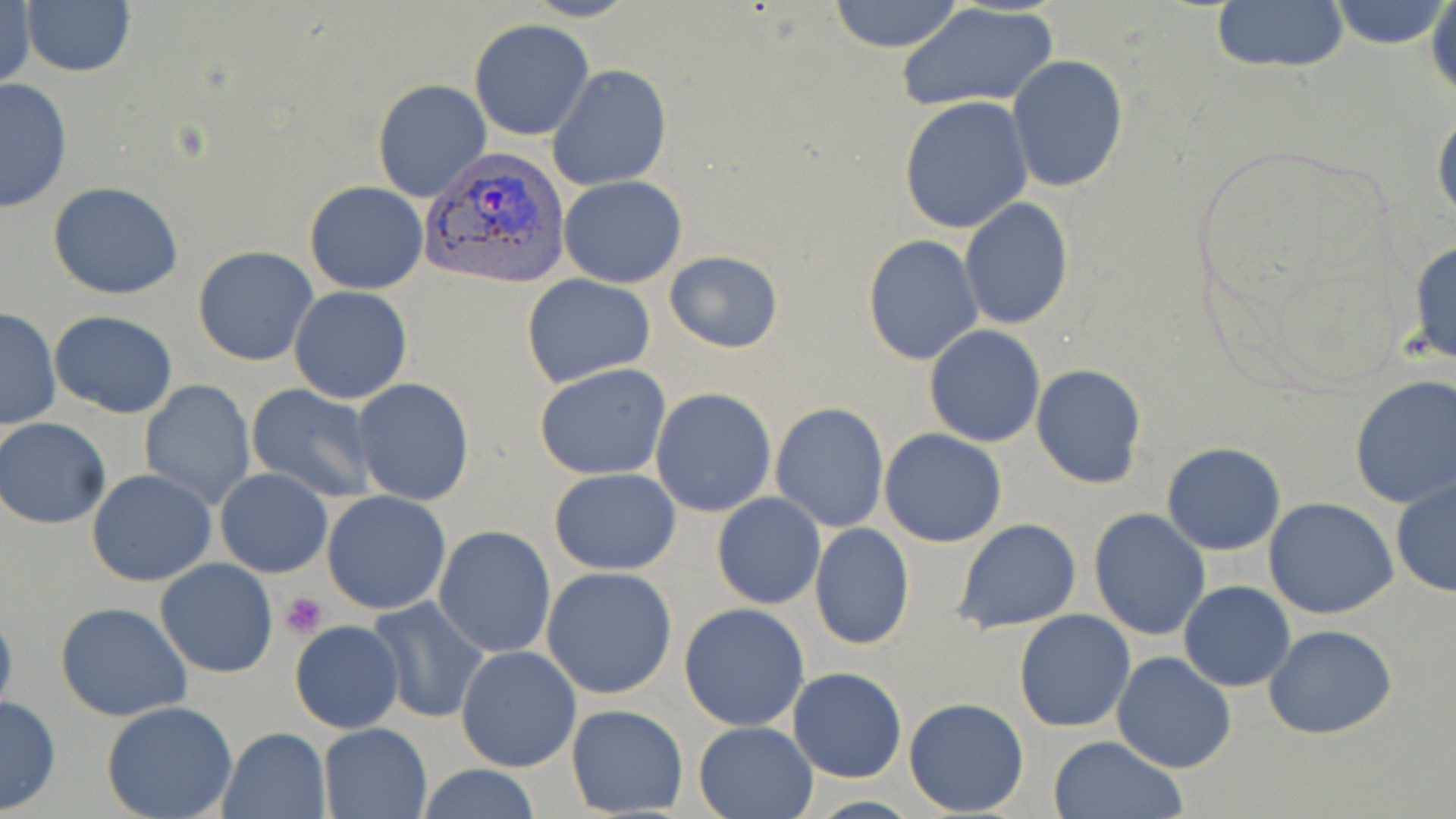

Summary:
  - Coordinate format: approximate bounding boxes as named x1/y1/x2/y2 corners in pixels
  - Platelet locations: (x1=279, y1=591, x2=329, y2=637)
  - Plasmodium vivax-infected red blood cell locations: (x1=420, y1=149, x2=572, y2=289)
  - Uninfected red blood cell locations: (x1=828, y1=0, x2=966, y2=52), (x1=1327, y1=0, x2=1451, y2=50), (x1=1429, y1=0, x2=1456, y2=101), (x1=1208, y1=1, x2=1350, y2=76), (x1=1, y1=2, x2=35, y2=94), (x1=21, y1=2, x2=136, y2=78), (x1=897, y1=3, x2=1059, y2=112), (x1=469, y1=20, x2=595, y2=140), (x1=1006, y1=54, x2=1129, y2=192), (x1=548, y1=66, x2=672, y2=191), (x1=0, y1=77, x2=74, y2=214), (x1=372, y1=80, x2=492, y2=202), (x1=901, y1=96, x2=1034, y2=234), (x1=1431, y1=102, x2=1456, y2=230), (x1=559, y1=174, x2=688, y2=288), (x1=305, y1=181, x2=428, y2=294), (x1=47, y1=182, x2=185, y2=299), (x1=959, y1=197, x2=1073, y2=330), (x1=863, y1=235, x2=983, y2=365), (x1=1407, y1=239, x2=1456, y2=368), (x1=193, y1=245, x2=319, y2=366), (x1=664, y1=250, x2=783, y2=354), (x1=522, y1=273, x2=655, y2=387), (x1=288, y1=285, x2=413, y2=404), (x1=0, y1=308, x2=61, y2=430), (x1=49, y1=311, x2=179, y2=419), (x1=924, y1=325, x2=1046, y2=447), (x1=535, y1=364, x2=673, y2=480), (x1=1030, y1=364, x2=1147, y2=489), (x1=1349, y1=376, x2=1456, y2=508), (x1=352, y1=379, x2=474, y2=505), (x1=138, y1=380, x2=256, y2=510), (x1=246, y1=384, x2=379, y2=503), (x1=651, y1=387, x2=778, y2=517), (x1=771, y1=402, x2=890, y2=533), (x1=1, y1=418, x2=112, y2=529), (x1=879, y1=428, x2=1007, y2=548), (x1=1161, y1=443, x2=1285, y2=556), (x1=215, y1=468, x2=332, y2=578), (x1=549, y1=468, x2=682, y2=575), (x1=86, y1=470, x2=219, y2=586), (x1=1390, y1=476, x2=1455, y2=598), (x1=322, y1=490, x2=452, y2=614), (x1=713, y1=491, x2=826, y2=610), (x1=1264, y1=497, x2=1398, y2=620), (x1=1088, y1=509, x2=1211, y2=641), (x1=952, y1=519, x2=1081, y2=633), (x1=809, y1=522, x2=915, y2=651), (x1=433, y1=525, x2=555, y2=658), (x1=154, y1=558, x2=278, y2=678), (x1=541, y1=566, x2=678, y2=700), (x1=1178, y1=581, x2=1294, y2=691), (x1=363, y1=596, x2=491, y2=723), (x1=0, y1=599, x2=18, y2=723), (x1=55, y1=602, x2=191, y2=721), (x1=680, y1=602, x2=810, y2=731), (x1=1014, y1=609, x2=1137, y2=732), (x1=289, y1=621, x2=406, y2=735), (x1=1264, y1=624, x2=1397, y2=741), (x1=456, y1=645, x2=581, y2=771), (x1=1111, y1=652, x2=1236, y2=773), (x1=788, y1=667, x2=907, y2=782), (x1=0, y1=695, x2=62, y2=815), (x1=904, y1=697, x2=1029, y2=817), (x1=100, y1=701, x2=239, y2=819), (x1=566, y1=704, x2=689, y2=816), (x1=693, y1=720, x2=818, y2=818), (x1=317, y1=722, x2=435, y2=818), (x1=218, y1=727, x2=330, y2=818), (x1=1049, y1=736, x2=1187, y2=819), (x1=415, y1=764, x2=543, y2=818)
  - Slide-level diagnosis: Plasmodium vivax
  - Magnification: 1000x
  - Preparation: thin blood film
  - Image size: 1456×819 pixels
  - Stain: May-Grünwald-Giemsa
  - Modality: light microscopy
  - Field of view: single